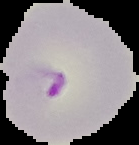
Summary:
  - Result: malaria parasites identified
  - Image type: segmented cell region with the area outside set to black
  - Preparation: thin blood smear
  - Image size: 139×145 pixels